State which parasite is depicted.
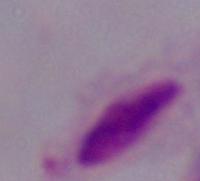

This is a trichomonad.

Captured at 1000x magnification. Photomicrograph.